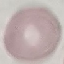
Summary:
  - Result: negative for malaria parasites
  - Preparation: thin blood smear
  - Capture: smartphone through the microscope eyepiece
  - Stain: Giemsa
  - Image type: cell patch, automatically extracted from a larger field of view and resized to 64 × 64 pixels